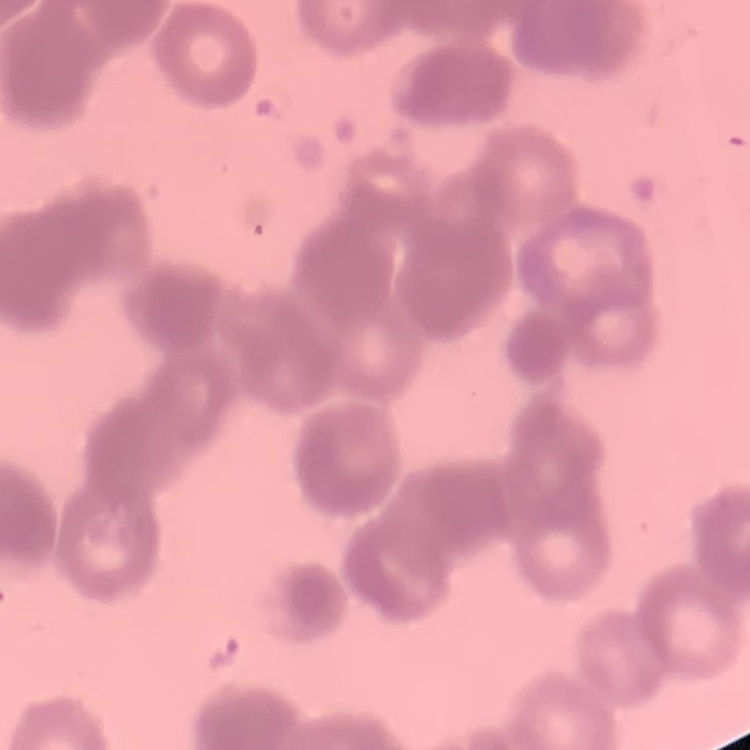
Summary:
  - Red blood cell morphology: rouleaux formation
  - Stain: Field's or Giemsa
  - Image type: one tile cut from a larger photomicrograph
  - Preparation: thin peripheral smear